Give the extent of all Plasmodium falciparum-infected red blood cells.
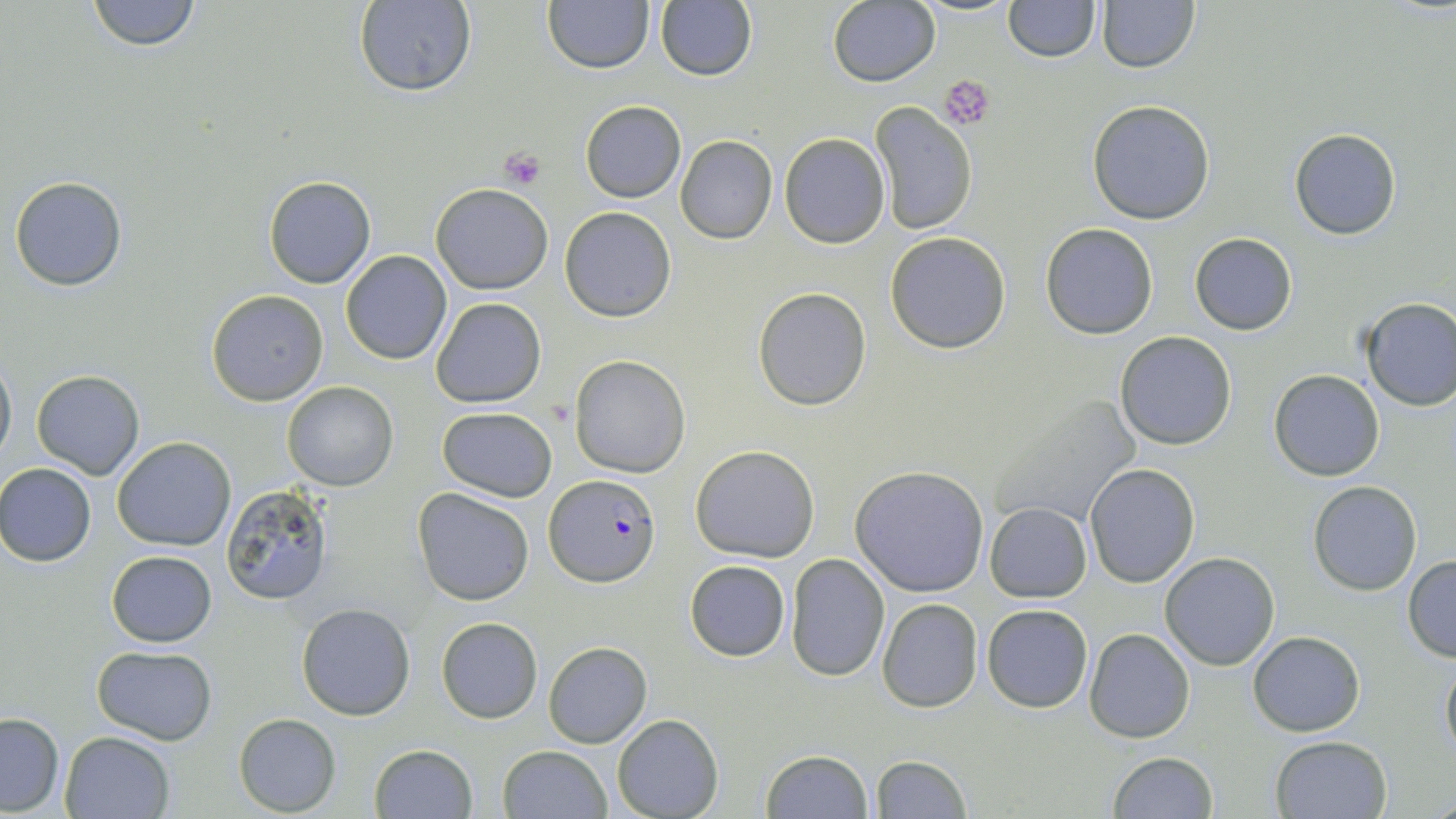
Approximate bounding boxes as (x1,y1)-(x2,y2) corner pairs in pixels.
Plasmodium falciparum-infected red blood cells: (545,474)-(661,586).

Summary:
  - Platelet locations: (941,74)-(997,129), (499,147)-(548,189)
  - Uninfected red blood cell locations: (87,0)-(201,51), (542,0)-(653,73), (1004,0)-(1100,61), (1096,0)-(1199,72), (353,1)-(477,95), (655,1)-(756,82), (827,2)-(939,86), (1087,99)-(1216,225), (580,102)-(685,202), (870,103)-(977,235), (1289,129)-(1401,240), (780,133)-(889,248), (675,135)-(777,243), (10,176)-(127,290), (264,176)-(377,288), (431,183)-(554,295), (560,206)-(677,322), (1041,223)-(1158,339), (885,232)-(1011,354), (1190,232)-(1296,334), (340,250)-(452,364), (754,288)-(871,410), (206,289)-(328,406), (431,297)-(546,409), (1358,297)-(1455,412), (1114,331)-(1237,449), (0,354)-(15,464), (571,355)-(689,476), (30,369)-(145,479), (1269,369)-(1385,481), (283,381)-(398,491), (979,391)-(1146,530), (438,406)-(556,501), (113,436)-(237,551), (691,444)-(820,563), (1084,462)-(1200,587), (0,465)-(97,565), (850,466)-(989,596), (1308,481)-(1422,596), (222,485)-(335,606), (411,488)-(535,606), (984,502)-(1092,602), (108,550)-(217,647), (787,552)-(891,683), (1160,552)-(1280,671), (1401,556)-(1456,662), (684,560)-(791,661), (877,599)-(983,713), (297,602)-(416,720), (981,604)-(1093,713), (437,617)-(542,723), (1084,629)-(1194,743), (1247,631)-(1364,735), (543,642)-(651,749), (92,645)-(216,743), (1440,653)-(1456,762), (0,712)-(65,814), (612,713)-(723,818), (234,714)-(340,816), (60,731)-(177,819), (1269,735)-(1392,818), (369,744)-(478,819), (498,745)-(613,819), (759,749)-(873,819), (1106,752)-(1218,819), (869,754)-(970,818)
  - Slide-level diagnosis: Plasmodium falciparum
  - Magnification: 1000x
  - Stain: May-Grünwald-Giemsa
  - Image size: 1456×819 pixels
  - Modality: light microscopy
  - Preparation: thin blood film
  - Field of view: one of a larger specimen